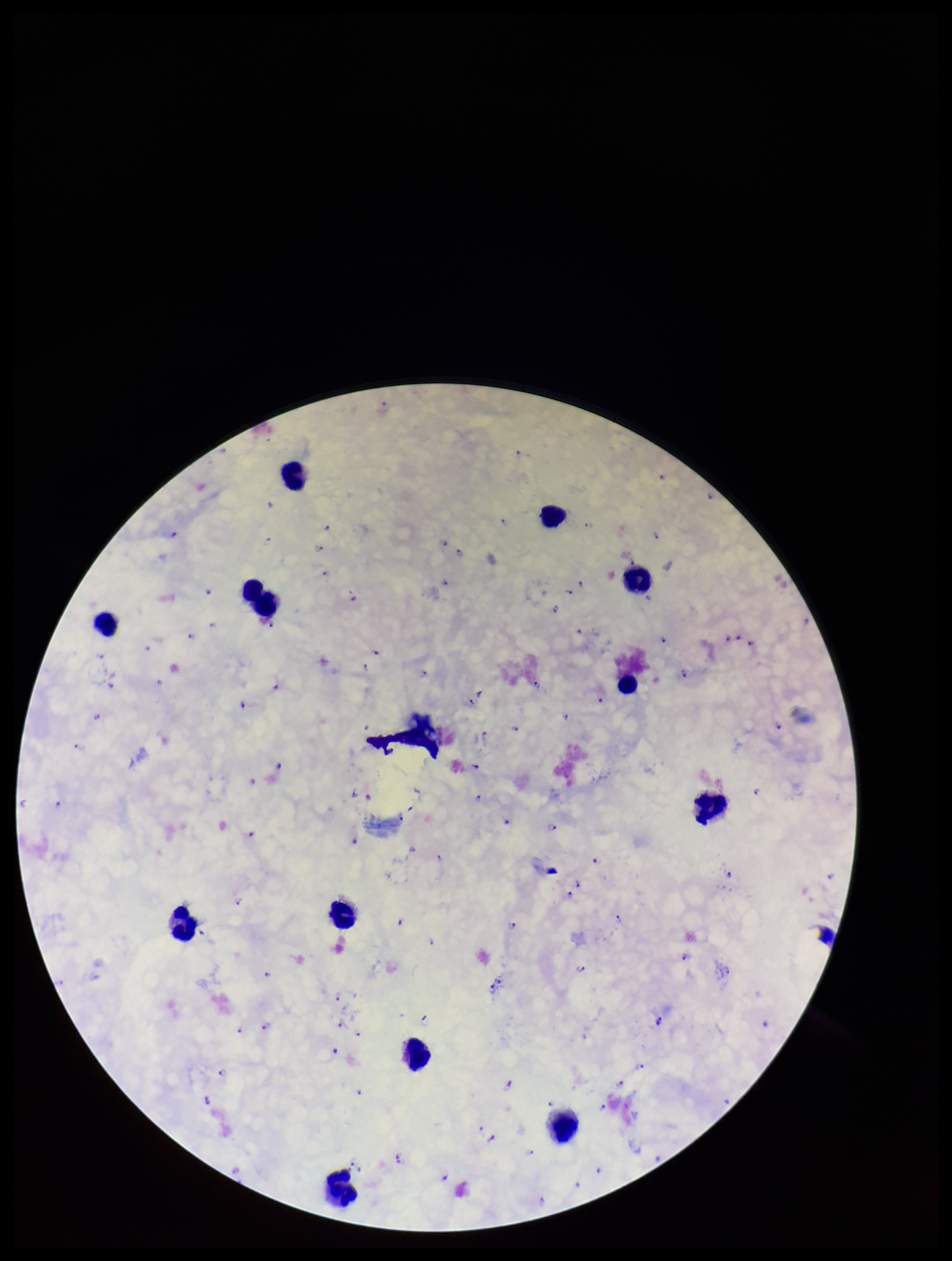 Single field of view. Patient malaria status: positive. Species reported for this patient: Plasmodium falciparum. Plasmodium parasites: identified. Leukocyte count: 13. Stained with Giemsa. Photographed through the microscope eyepiece with a smartphone camera. Preparation: thick blood smear. Image is 952×1261 pixels. Parasite count: 114.